Mark where platelets are.
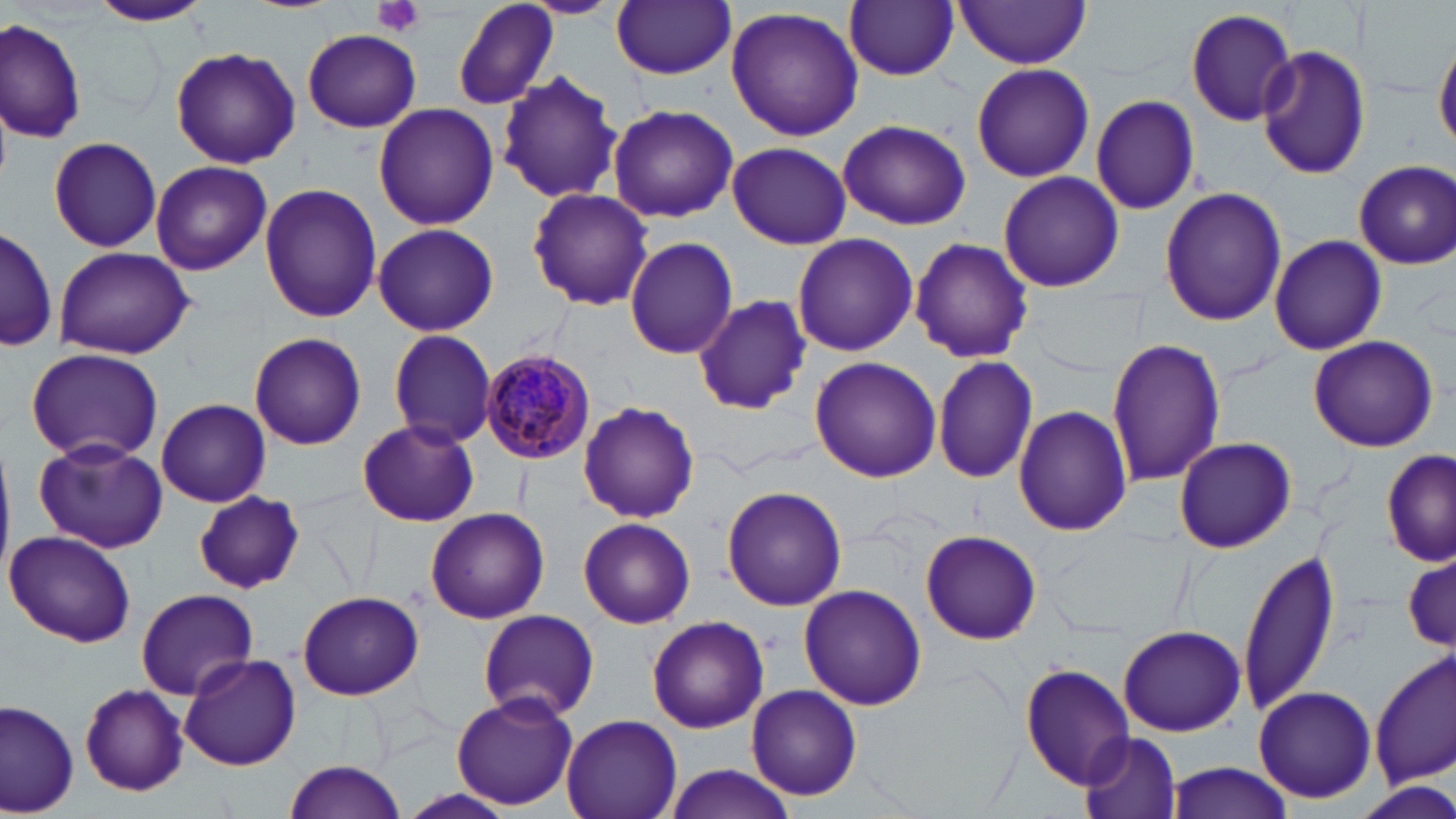

Approximate bounding boxes as (x1,y1)-(x2,y2) corner pairs in pixels.
Platelets: (375,0)-(425,37).

slide_level_diagnosis: Plasmodium malariae
preparation: thin blood smear
magnification: 1000x
uninfected_red_blood_cell_locations: 'approximate bounding boxes as (x1,y1)-(x2,y2) corner pairs in pixels: (451,0)-(560,111), (522,0)-(619,18), (89,1)-(212,28), (613,1)-(736,78), (845,1)-(959,81), (953,2)-(1092,68), (724,6)-(864,141), (1185,7)-(1299,126), (0,17)-(85,141), (302,29)-(422,132), (1433,35)-(1456,156), (1255,45)-(1372,180), (169,46)-(300,170), (971,63)-(1096,183), (496,71)-(624,205), (1091,96)-(1200,214), (372,101)-(500,230), (607,103)-(739,222), (837,118)-(972,231), (615,122)-(739,325), (46,137)-(164,252), (725,141)-(851,248), (150,160)-(271,276), (1353,161)-(1455,268), (997,171)-(1125,292), (259,182)-(381,324), (1159,187)-(1287,328), (526,189)-(655,312), (755,199)-(891,335), (371,222)-(500,337), (1,224)-(58,354), (791,233)-(918,357), (1269,234)-(1388,355), (623,237)-(737,359), (911,237)-(1033,363), (52,245)-(196,359), (693,295)-(812,414), (386,329)-(498,448), (248,332)-(367,449), (1308,335)-(1438,452), (1105,336)-(1226,487), (25,348)-(164,463), (932,353)-(1040,484), (808,357)-(942,484), (156,398)-(271,508), (578,400)-(700,524), (1014,404)-(1131,537), (356,419)-(480,527), (1172,435)-(1297,554), (34,437)-(168,554), (1382,452)-(1456,566), (723,486)-(848,612), (195,491)-(304,593), (424,505)-(549,623), (578,517)-(695,629), (920,529)-(1041,643), (3,530)-(137,647), (1241,546)-(1341,717), (1403,553)-(1455,653), (798,585)-(927,711), (135,588)-(258,700), (295,589)-(426,701), (476,609)-(600,723), (646,615)-(769,733), (1118,623)-(1245,736), (1371,648)-(1455,788), (179,652)-(301,771), (1020,662)-(1135,790), (746,683)-(864,801), (79,685)-(189,795), (1252,685)-(1378,805), (450,692)-(578,811), (2,699)-(79,817), (561,715)-(682,819), (1080,733)-(1181,819), (282,761)-(407,819), (1162,761)-(1295,819), (659,763)-(803,819)'
plasmodium_malariae_infected_red_blood_cell_locations: 'approximate bounding boxes as (x1,y1)-(x2,y2) corner pairs in pixels: (480,347)-(596,462)'
modality: light microscopy
stain: May-Grünwald-Giemsa
field_of_view: single
image_size: 1456×819 pixels